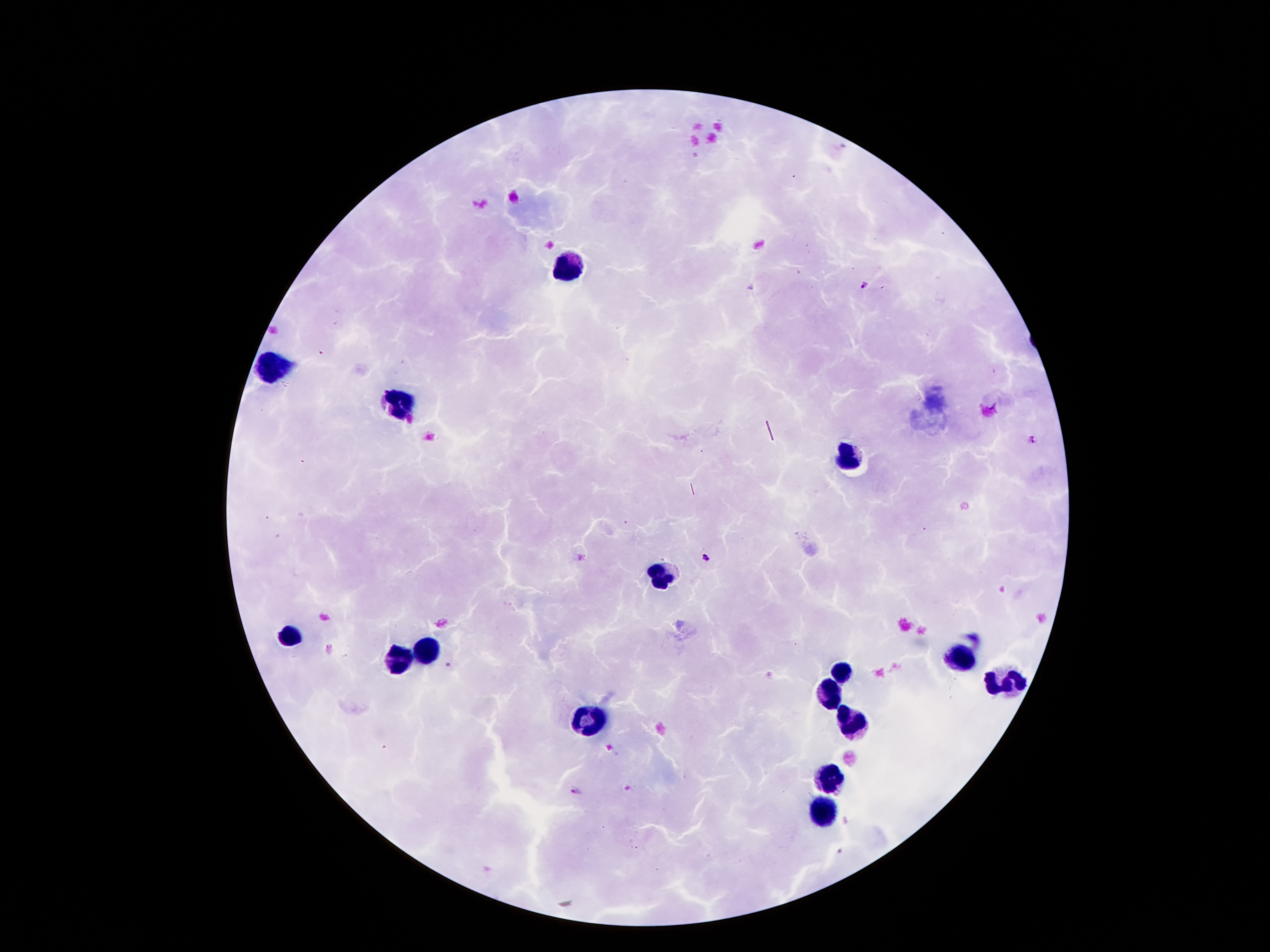

coordinate format = approximate centers as {x, y} in pixels
malaria parasite locations = {864, 288}, {1032, 440}, {705, 558}, {448, 665}, {575, 793}
leukocyte locations = {569, 266}, {273, 365}, {399, 407}, {846, 456}, {661, 572}, {290, 637}, {426, 651}, {404, 656}, {957, 659}, {841, 671}, {1002, 681}, {826, 693}, {849, 720}, {589, 723}, {831, 780}, {821, 809}
preparation = thick peripheral-blood smear
magnification = 100x
patient malaria status = positive for Plasmodium falciparum
stain = Giemsa
capture = smartphone camera through the microscope eyepiece
field of view = single
image size = 1270×952 pixels